Classify this cell by malaria status.
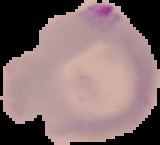
Parasitized.

From a thin blood film. Cell region segmented out of the field of view; the surrounding area is masked to black. Image is 160×145 pixels.